Report the malaria status of this cell.
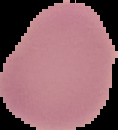

It is uninfected.

Summary:
  - Preparation: thin blood film
  - Image size: 118×130 pixels
  - Image type: segmented cell region with the area outside set to black